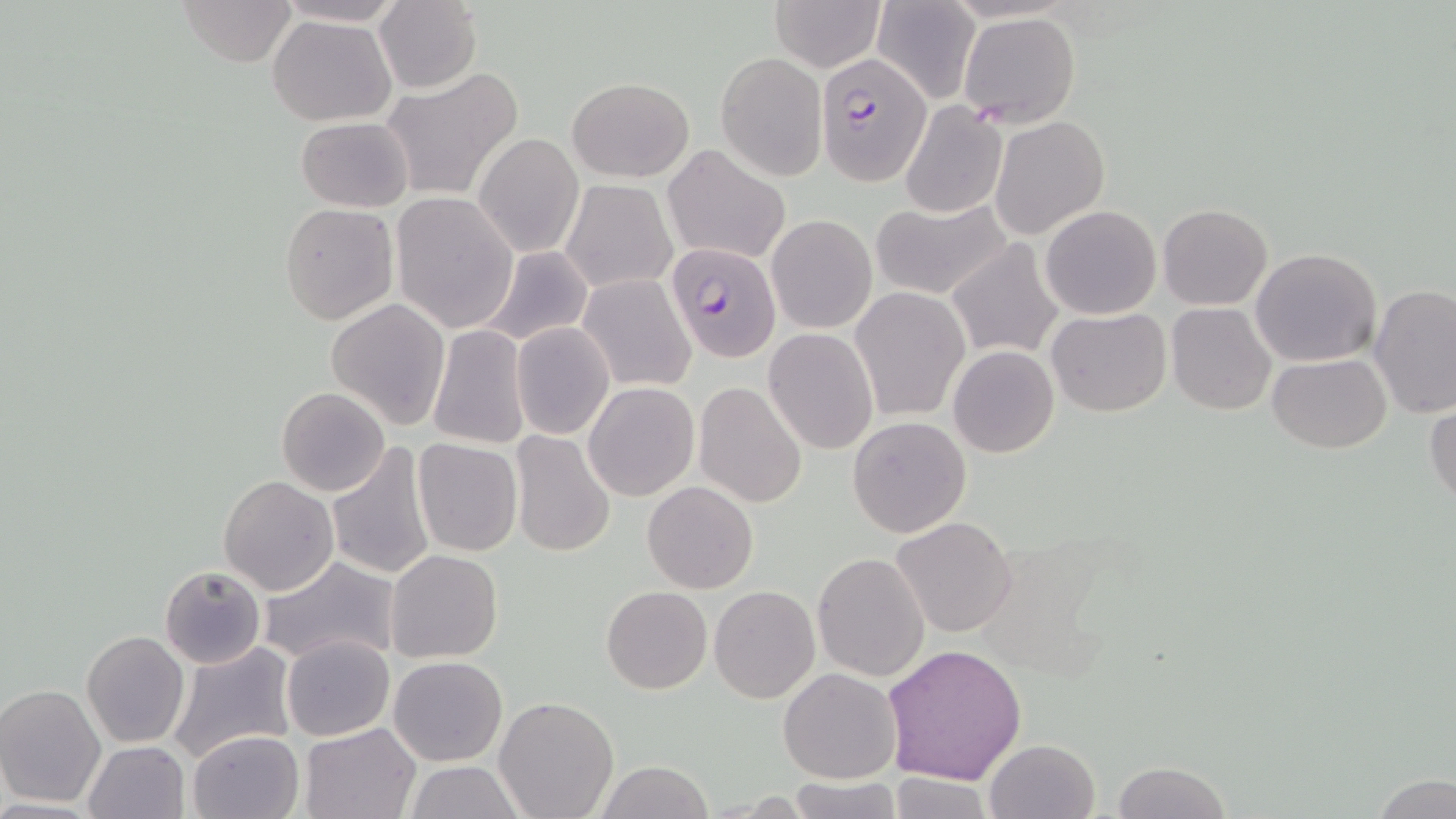 Approximate bounding boxes as (x1, y1, x2, y2) in pixels. Plasmodium falciparum-infected red blood cell locations: (814, 55, 930, 182), (665, 243, 782, 363). Uninfected red blood cell locations: (179, 0, 297, 67), (274, 0, 407, 27), (770, 0, 883, 73), (871, 0, 981, 103), (374, 1, 484, 95), (957, 11, 1080, 128), (267, 14, 396, 125), (716, 53, 825, 180), (385, 65, 526, 200), (566, 75, 693, 182), (898, 100, 1009, 219), (294, 115, 414, 213), (989, 116, 1110, 239), (475, 133, 583, 258), (662, 145, 791, 265), (562, 180, 675, 293), (391, 192, 518, 334), (869, 197, 1013, 302), (277, 202, 399, 326), (1157, 203, 1272, 310), (1040, 204, 1163, 319), (766, 213, 877, 334), (945, 238, 1066, 361), (478, 245, 595, 348), (1250, 246, 1383, 367), (578, 274, 696, 392), (1370, 283, 1456, 418), (849, 287, 971, 421), (326, 298, 450, 430), (1167, 302, 1277, 415), (1047, 307, 1170, 417), (510, 322, 615, 440), (427, 325, 532, 449), (763, 329, 878, 455), (948, 346, 1060, 459), (1268, 354, 1392, 453), (583, 382, 699, 501), (693, 382, 808, 508), (276, 387, 390, 496), (1425, 399, 1456, 511), (846, 415, 971, 538), (509, 432, 615, 557), (413, 438, 523, 556), (325, 440, 436, 579), (217, 475, 338, 595), (642, 480, 758, 594), (889, 516, 1017, 639), (385, 549, 504, 662), (811, 551, 929, 683), (258, 555, 401, 666), (158, 564, 267, 669), (709, 585, 821, 703), (602, 586, 712, 694), (80, 629, 190, 749), (280, 635, 395, 741), (165, 642, 297, 764), (882, 642, 1028, 785), (389, 656, 507, 766), (779, 667, 903, 784), (0, 683, 106, 808), (494, 696, 619, 819), (299, 722, 421, 818), (188, 729, 304, 819), (984, 738, 1100, 819), (83, 739, 191, 818), (403, 760, 526, 818), (597, 760, 712, 819), (1112, 760, 1232, 818), (884, 772, 995, 818), (1369, 772, 1456, 819), (787, 775, 908, 818). Slide-level diagnosis: Plasmodium falciparum. One field of a larger specimen. Captured at 1000x magnification. Image is 1456×819 pixels. Thin blood film. Optical microscopy. May-Grünwald-Giemsa-stained preparation.